Report the malaria status of this cell.
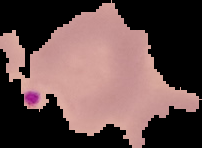
Parasitized.

Summary:
  - Image type: segmented cell region with the area outside set to black
  - Image size: 202×148 pixels
  - Preparation: thin blood film